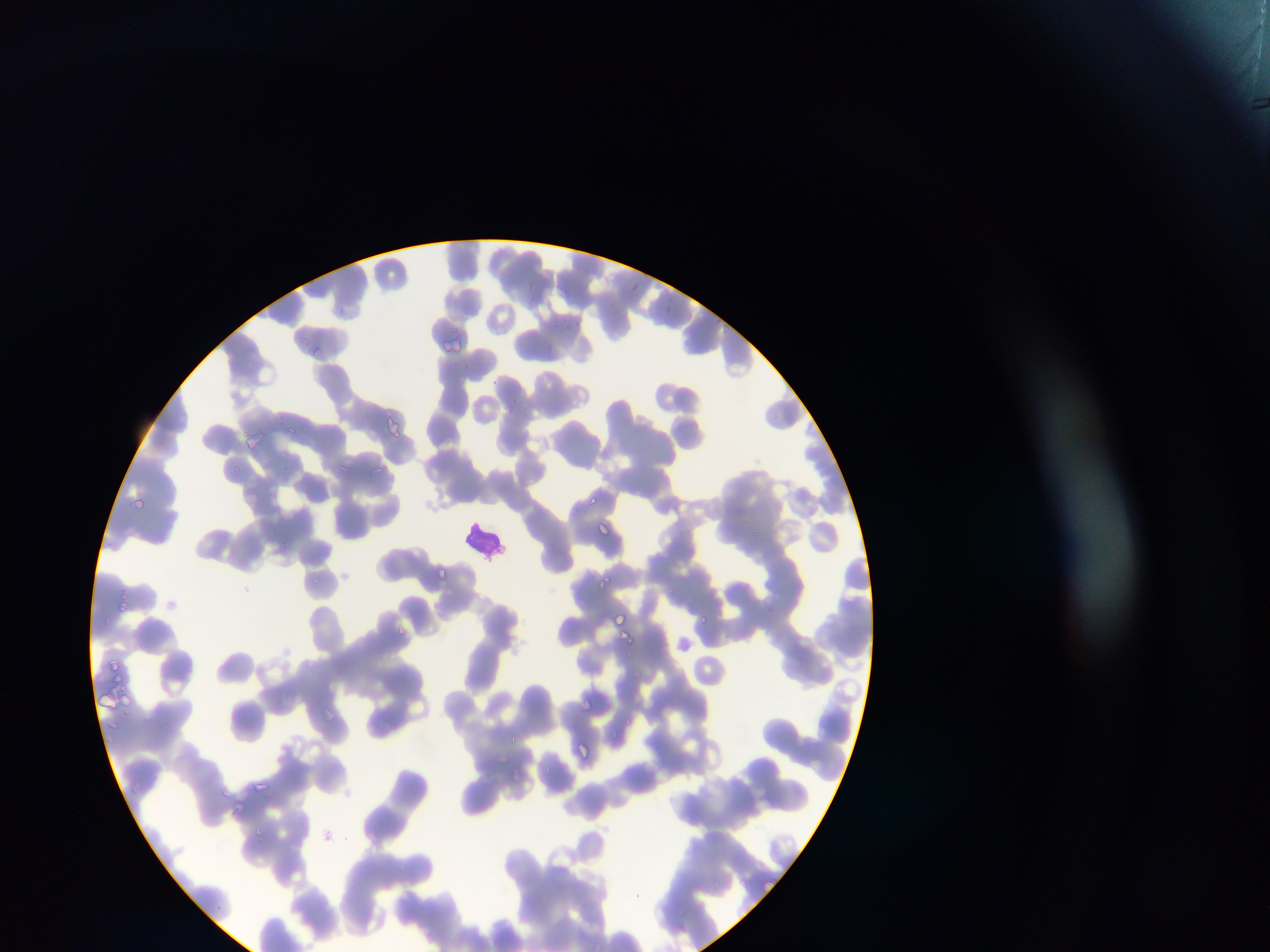
Approximate bounding boxes as [left, top, right, bottom] in pixels.
Summary:
  - Malaria parasite locations: [722, 325, 736, 338], [447, 328, 460, 335], [506, 404, 515, 416], [383, 416, 407, 439], [588, 495, 605, 512], [133, 498, 146, 511], [735, 507, 742, 518], [595, 523, 606, 539], [751, 530, 758, 541], [283, 541, 292, 550], [437, 568, 449, 580], [313, 576, 320, 585], [592, 576, 608, 590], [666, 584, 681, 598], [120, 601, 128, 610], [613, 606, 628, 628], [695, 615, 717, 625], [399, 626, 408, 640], [619, 632, 637, 651], [626, 717, 638, 735]
  - Image size: 1270×952 pixels
  - Capture: mobile-phone photograph through a microscope
  - Preparation: thin blood film
  - Country: Ghana
  - Field of view: single